Give the position of every malaria parasite.
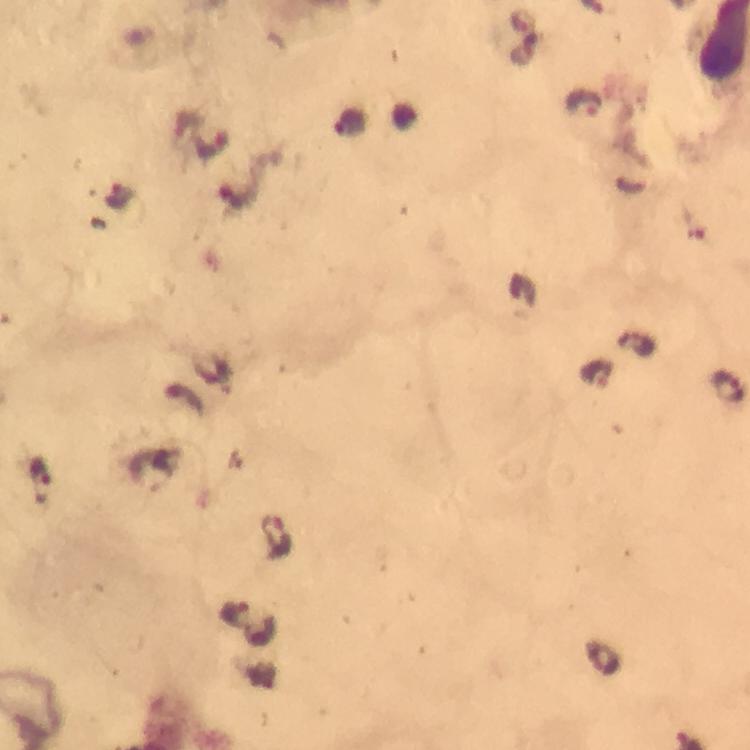
Approximate centers as (x, y) in pixels.
Malaria parasites: (584, 104), (117, 196), (235, 196), (729, 386), (40, 478), (276, 534), (234, 613).

Summary:
  - Image size: 750×750 pixels
  - Capture: smartphone mounted on the microscope
  - Preparation: thick blood film
  - Cropped from: one field of view
  - Stain: Giemsa
  - Magnification: 100x
  - Context: from a diagnostic examination for malaria
  - Immersion oil: applied